Give the position of every malaria parasite and every leukocyte.
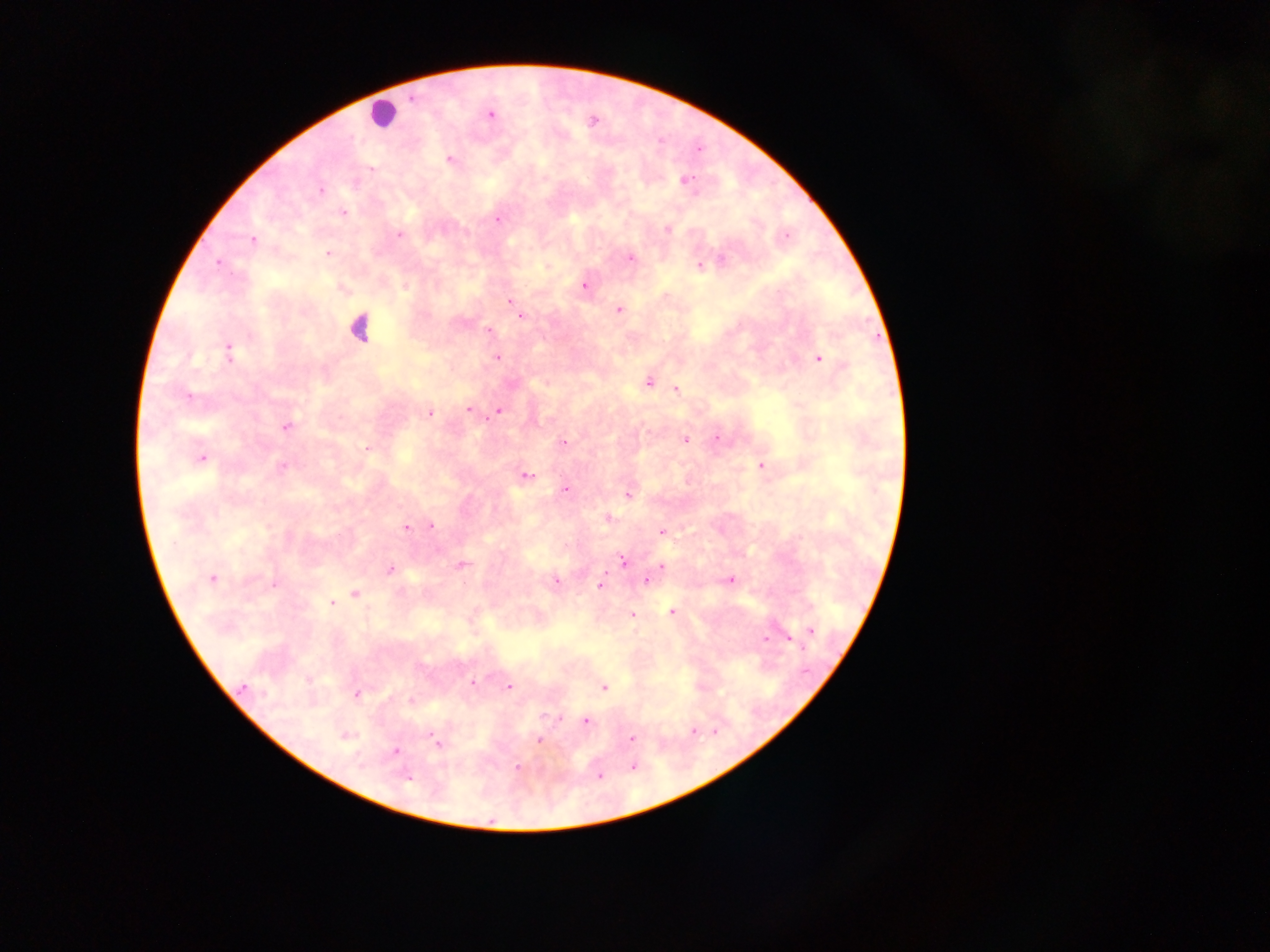

Approximate centers as x y in pixels.
Malaria parasites: 411 98; 490 114; 450 158; 371 168; 685 180; 320 190; 344 213; 498 220; 667 229; 400 235; 785 236; 252 240; 329 254; 630 258; 722 258; 219 262; 700 266; 584 285; 405 287; 510 301; 619 310; 521 317; 489 331; 229 351; 498 357; 819 358; 648 383; 676 390; 189 396; 468 410; 499 411; 429 413; 286 427; 718 438; 685 440; 563 442; 366 449; 203 458; 761 465; 282 467; 526 475; 565 489; 628 494; 608 518; 431 525; 406 529; 662 532; 623 560; 462 564; 662 565; 389 569; 212 579; 646 580; 730 580; 557 581; 274 585; 600 585; 355 594; 331 603; 672 612; 632 615; 811 630; 766 639; 790 641; 472 682; 244 687; 509 687; 604 688; 356 694; 411 700; 586 721; 693 731; 346 736; 631 738; 539 740; 438 743; 395 751; 633 767; 517 768; 600 776; 408 778.
Leukocytes: 382 114; 360 329.

Summary:
  - Image size: 1270×952 pixels
  - Capture: mobile-phone photograph through a microscope
  - Preparation: thick blood smear
  - Country: Ghana
  - Field of view: single